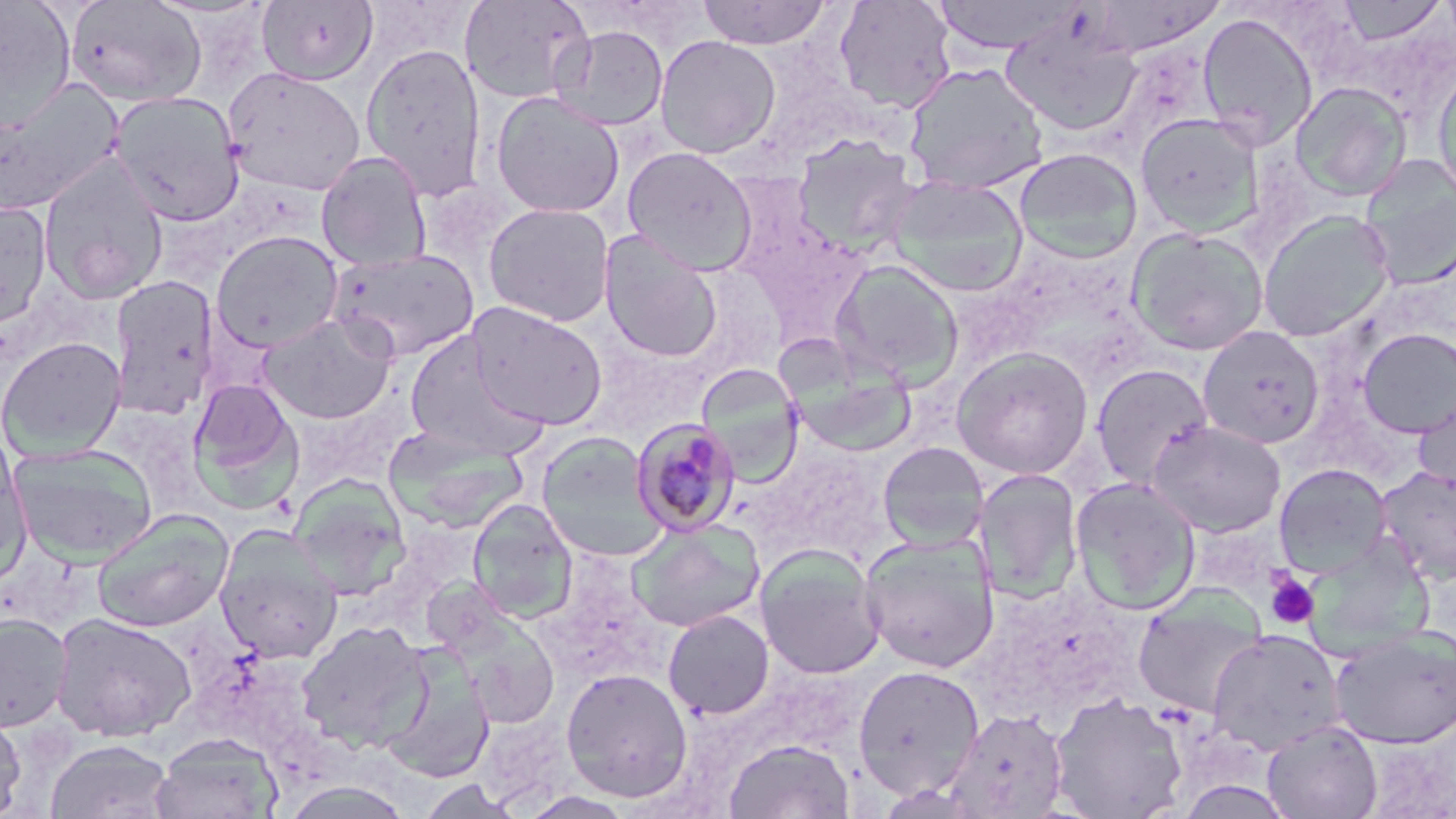

slide-level diagnosis = Plasmodium malariae
image size = 1456×819 pixels
stain = May-Grünwald-Giemsa
magnification = 1000x
preparation = thin blood smear
field of view = single
uninfected red blood cell locations = approximate bounding boxes as (x1,y1)-(x2,y2) corner pairs in pixels: (256,0)-(378,86), (459,0)-(594,104), (697,0)-(833,49), (833,0)-(957,114), (930,0)-(1083,54), (1086,0)-(1227,56), (1336,0)-(1447,44), (0,1)-(76,131), (65,1)-(206,105), (1197,12)-(1318,148), (1001,22)-(1143,136), (554,24)-(668,131), (655,34)-(781,158), (360,42)-(486,202), (903,62)-(1050,195), (1432,66)-(1456,204), (222,67)-(366,197), (0,79)-(123,216), (1290,82)-(1412,201), (110,91)-(245,226), (490,92)-(625,218), (1136,113)-(1263,237), (791,133)-(922,256), (621,146)-(758,275), (1014,148)-(1142,263), (316,151)-(432,272), (1359,155)-(1456,290), (38,156)-(169,304), (887,176)-(1029,297), (0,200)-(52,329), (483,203)-(615,327), (1257,210)-(1395,342), (1126,227)-(1269,356), (210,230)-(344,352), (599,231)-(722,363), (329,249)-(479,363), (830,259)-(964,389), (110,276)-(219,419), (468,302)-(609,430), (258,314)-(396,423), (1198,325)-(1324,448), (1357,328)-(1456,439), (403,334)-(546,459), (0,336)-(126,461), (951,346)-(1094,479), (1091,363)-(1213,489), (695,364)-(804,483), (188,379)-(300,502), (1413,391)-(1456,499), (1147,420)-(1286,537), (384,426)-(529,533), (0,432)-(30,576), (537,433)-(666,559), (877,441)-(988,552), (6,443)-(157,566), (1274,463)-(1392,577), (1376,465)-(1456,585), (973,468)-(1083,603), (1069,476)-(1202,615), (288,477)-(410,599), (467,500)-(578,622), (92,508)-(234,632), (626,520)-(764,633), (213,524)-(344,665), (859,533)-(999,673), (756,546)-(885,679), (1133,587)-(1267,720), (663,609)-(774,719), (51,612)-(197,742), (0,613)-(72,731), (455,615)-(560,727), (296,619)-(431,751), (1329,625)-(1456,749), (1206,628)-(1347,755), (380,653)-(495,784), (852,664)-(985,800), (561,667)-(693,802), (1048,691)-(1189,819), (0,706)-(26,819), (945,709)-(1069,818), (1261,720)-(1383,819), (151,733)-(282,819), (46,739)-(175,819), (725,739)-(854,818), (418,779)-(519,818), (280,780)-(415,819)
Plasmodium malariae-infected red blood cell locations = approximate bounding boxes as (x1,y1)-(x2,y2) corner pairs in pixels: (629,418)-(742,537)
modality = optical microscopy
platelet locations = approximate bounding boxes as (x1,y1)-(x2,y2) corner pairs in pixels: (1264,572)-(1320,629)